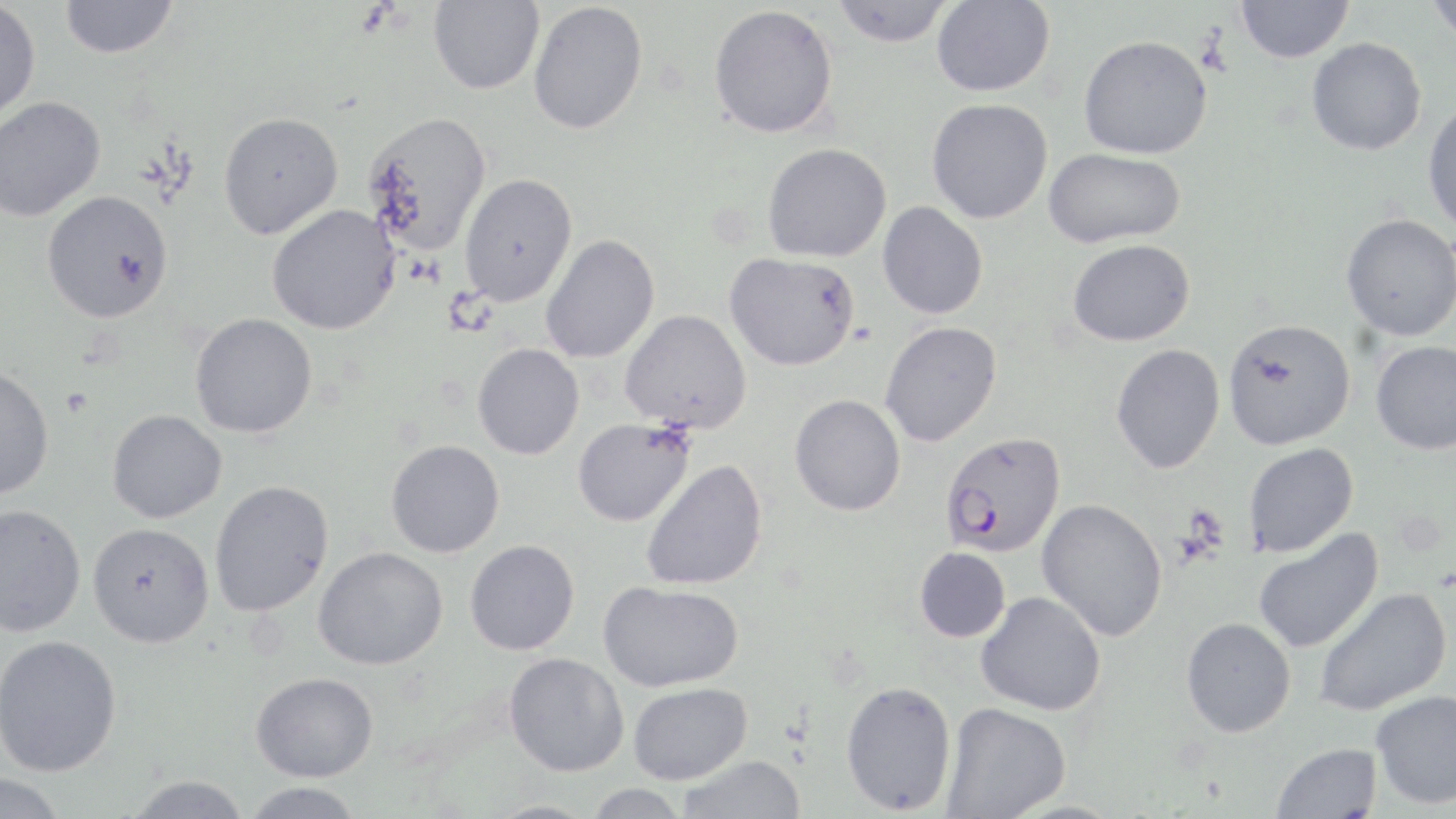
slide_level_diagnosis: Plasmodium falciparum
field_of_view: one of a larger specimen
image_size: 1456×819 pixels
preparation: thin blood smear
plasmodium_falciparum_infected_red_blood_cell_locations: 'approximate bounding boxes as named x1/y1/x2/y2 corners in pixels: (x1=939, y1=431, x2=1066, y2=557)'
modality: optical microscopy
magnification: 1000x
uninfected_red_blood_cell_locations: 'approximate bounding boxes as named x1/y1/x2/y2 corners in pixels: (x1=60, y1=0, x2=179, y2=59), (x1=428, y1=0, x2=544, y2=94), (x1=830, y1=0, x2=955, y2=47), (x1=1424, y1=0, x2=1456, y2=46), (x1=0, y1=1, x2=40, y2=124), (x1=932, y1=1, x2=1055, y2=97), (x1=1235, y1=1, x2=1354, y2=63), (x1=528, y1=2, x2=648, y2=134), (x1=709, y1=4, x2=839, y2=138), (x1=1079, y1=34, x2=1213, y2=159), (x1=1306, y1=37, x2=1426, y2=155), (x1=0, y1=96, x2=105, y2=222), (x1=926, y1=98, x2=1053, y2=224), (x1=1423, y1=98, x2=1456, y2=235), (x1=218, y1=111, x2=343, y2=239), (x1=362, y1=111, x2=492, y2=257), (x1=763, y1=143, x2=892, y2=263), (x1=1044, y1=148, x2=1187, y2=248), (x1=458, y1=172, x2=577, y2=307), (x1=41, y1=190, x2=174, y2=324), (x1=877, y1=202, x2=988, y2=319), (x1=266, y1=204, x2=401, y2=335), (x1=1341, y1=214, x2=1456, y2=341), (x1=540, y1=234, x2=659, y2=364), (x1=1067, y1=239, x2=1195, y2=346), (x1=724, y1=252, x2=860, y2=371), (x1=620, y1=309, x2=751, y2=432), (x1=189, y1=313, x2=317, y2=438), (x1=1222, y1=318, x2=1355, y2=450), (x1=880, y1=321, x2=1002, y2=447), (x1=1371, y1=341, x2=1456, y2=455), (x1=472, y1=343, x2=584, y2=460), (x1=1111, y1=344, x2=1225, y2=474), (x1=0, y1=365, x2=54, y2=500), (x1=789, y1=394, x2=906, y2=516), (x1=107, y1=409, x2=227, y2=523), (x1=573, y1=417, x2=695, y2=526), (x1=386, y1=439, x2=505, y2=557), (x1=1242, y1=442, x2=1359, y2=557), (x1=640, y1=459, x2=768, y2=591), (x1=209, y1=480, x2=333, y2=617), (x1=1037, y1=498, x2=1168, y2=641), (x1=1, y1=503, x2=86, y2=637), (x1=87, y1=522, x2=214, y2=647), (x1=1253, y1=529, x2=1384, y2=654), (x1=464, y1=540, x2=579, y2=655), (x1=313, y1=546, x2=448, y2=670), (x1=914, y1=547, x2=1010, y2=643), (x1=598, y1=580, x2=744, y2=692), (x1=1314, y1=587, x2=1451, y2=716), (x1=976, y1=591, x2=1107, y2=716), (x1=1181, y1=617, x2=1297, y2=738), (x1=0, y1=635, x2=121, y2=776), (x1=504, y1=652, x2=630, y2=776), (x1=251, y1=671, x2=378, y2=781), (x1=840, y1=680, x2=957, y2=815), (x1=628, y1=682, x2=752, y2=785), (x1=1371, y1=690, x2=1456, y2=810), (x1=941, y1=702, x2=1071, y2=818), (x1=1271, y1=742, x2=1382, y2=818), (x1=678, y1=755, x2=805, y2=818), (x1=0, y1=774, x2=67, y2=819), (x1=124, y1=775, x2=252, y2=818), (x1=240, y1=782, x2=367, y2=818), (x1=584, y1=783, x2=691, y2=819), (x1=479, y1=800, x2=603, y2=818)'
stain: May-Grünwald-Giemsa